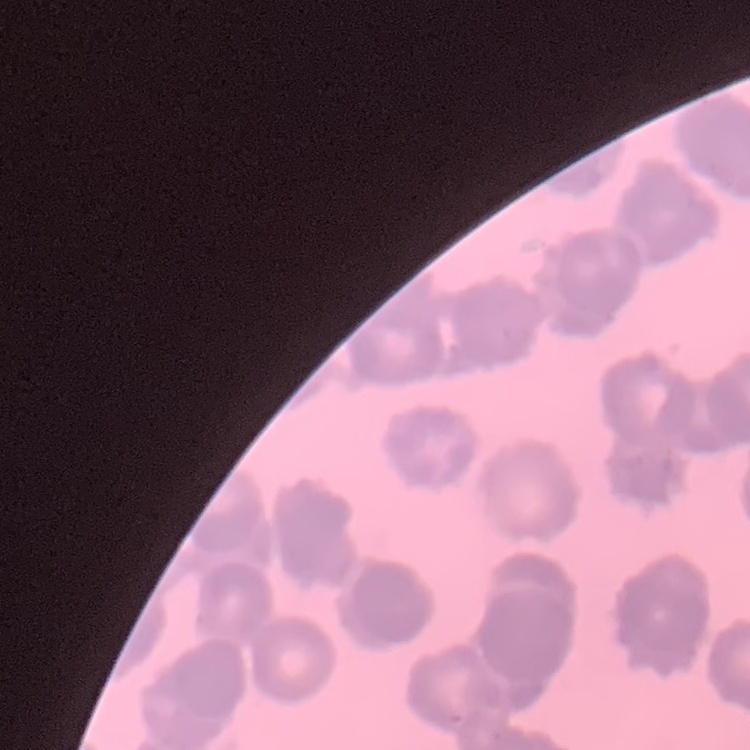
The erythrocytes exhibit rouleaux formation. Stained with either Field's or Giemsa. One tile cut from a larger photomicrograph. Thin blood smear.